Locate every blood parasite and identify its species.
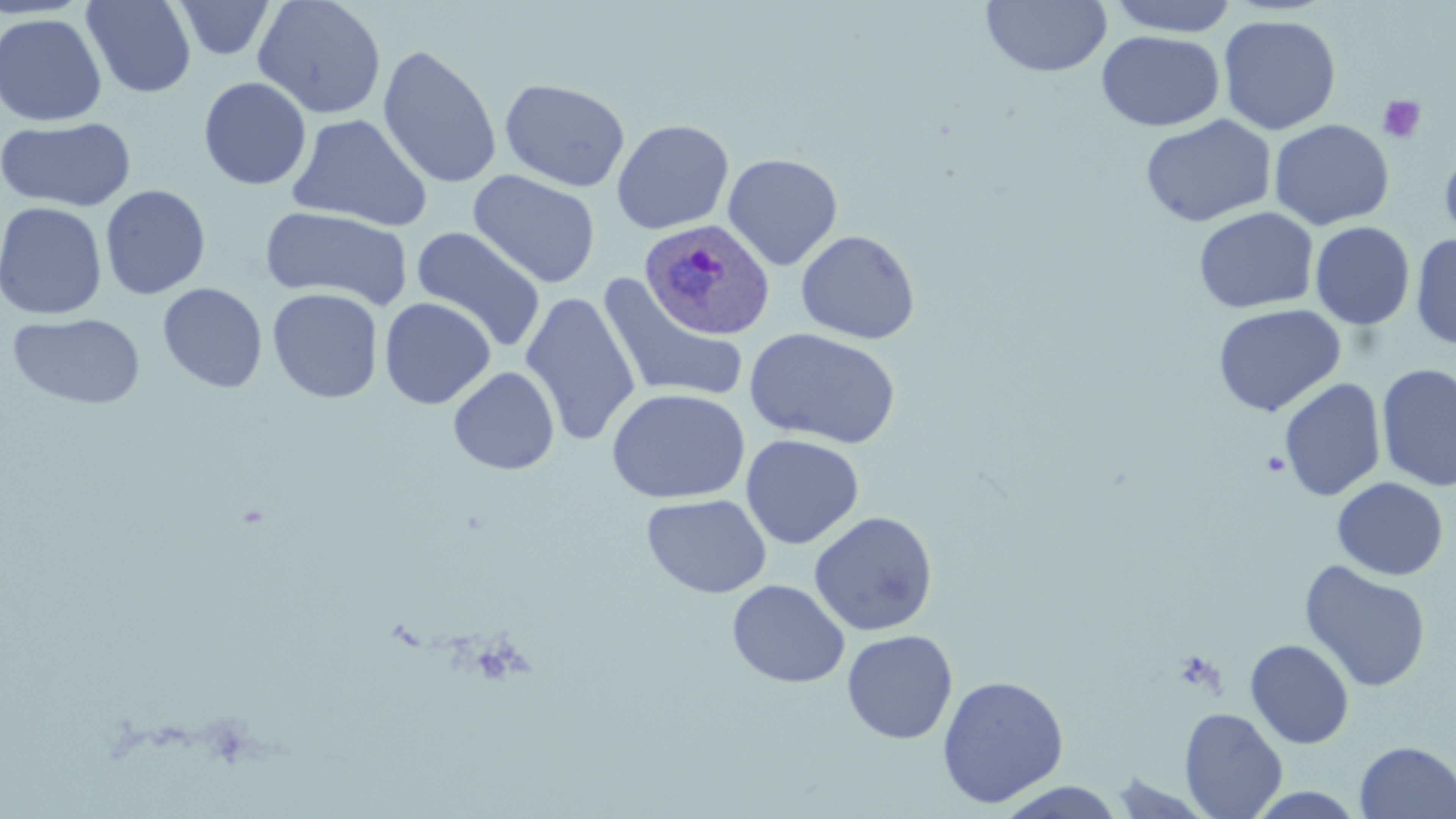

Approximate bounding boxes as named x1/y1/x2/y2 corners in pixels.
Plasmodium ovale-infected red blood cells: (x1=641, y1=220, x2=778, y2=342).
No Plasmodium falciparum, Plasmodium malariae, Plasmodium vivax, Babesia divergens, or Trypanosoma brucei observed.

Summary:
  - Platelet locations: (x1=1376, y1=93, x2=1427, y2=145), (x1=1261, y1=450, x2=1291, y2=476)
  - Uninfected red blood cell locations: (x1=171, y1=0, x2=277, y2=61), (x1=252, y1=0, x2=387, y2=119), (x1=981, y1=0, x2=1112, y2=78), (x1=1105, y1=0, x2=1241, y2=37), (x1=82, y1=1, x2=196, y2=98), (x1=0, y1=12, x2=107, y2=126), (x1=1217, y1=14, x2=1342, y2=135), (x1=1097, y1=30, x2=1225, y2=131), (x1=377, y1=44, x2=502, y2=189), (x1=198, y1=76, x2=312, y2=190), (x1=499, y1=78, x2=631, y2=192), (x1=286, y1=113, x2=433, y2=232), (x1=1141, y1=114, x2=1276, y2=228), (x1=1, y1=117, x2=137, y2=212), (x1=611, y1=118, x2=734, y2=234), (x1=1269, y1=119, x2=1394, y2=230), (x1=1439, y1=143, x2=1456, y2=250), (x1=722, y1=152, x2=843, y2=270), (x1=467, y1=170, x2=601, y2=288), (x1=99, y1=184, x2=211, y2=299), (x1=0, y1=201, x2=107, y2=320), (x1=261, y1=206, x2=414, y2=309), (x1=1193, y1=206, x2=1318, y2=314), (x1=1310, y1=221, x2=1415, y2=330), (x1=410, y1=226, x2=547, y2=353), (x1=795, y1=230, x2=920, y2=344), (x1=1410, y1=231, x2=1455, y2=351), (x1=596, y1=276, x2=750, y2=405), (x1=157, y1=283, x2=268, y2=393), (x1=267, y1=287, x2=383, y2=403), (x1=520, y1=291, x2=641, y2=447), (x1=379, y1=297, x2=496, y2=409), (x1=1212, y1=303, x2=1345, y2=416), (x1=7, y1=312, x2=146, y2=410), (x1=744, y1=328, x2=901, y2=448), (x1=1376, y1=363, x2=1456, y2=492), (x1=448, y1=366, x2=560, y2=475), (x1=1279, y1=377, x2=1386, y2=501), (x1=606, y1=387, x2=750, y2=504), (x1=741, y1=433, x2=864, y2=549), (x1=1331, y1=477, x2=1449, y2=581), (x1=641, y1=493, x2=772, y2=599), (x1=808, y1=511, x2=939, y2=636), (x1=1299, y1=560, x2=1432, y2=693), (x1=727, y1=579, x2=850, y2=688), (x1=841, y1=629, x2=958, y2=744), (x1=1245, y1=639, x2=1354, y2=748), (x1=937, y1=675, x2=1069, y2=807), (x1=1179, y1=707, x2=1287, y2=819), (x1=1355, y1=741, x2=1456, y2=819), (x1=1108, y1=773, x2=1219, y2=818), (x1=993, y1=782, x2=1128, y2=817), (x1=1244, y1=787, x2=1368, y2=818)
  - Slide-level diagnosis: Plasmodium ovale
  - Field of view: one of a larger specimen
  - Magnification: 1000x
  - Modality: light microscopy
  - Stain: May-Grünwald-Giemsa
  - Preparation: thin blood smear
  - Image size: 1456×819 pixels